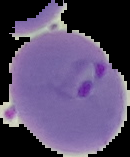

Summary:
  - Preparation: thin blood smear
  - Result: Plasmodium parasites detected
  - Image size: 130×157 pixels
  - Image type: segmented cell region with the area outside set to black